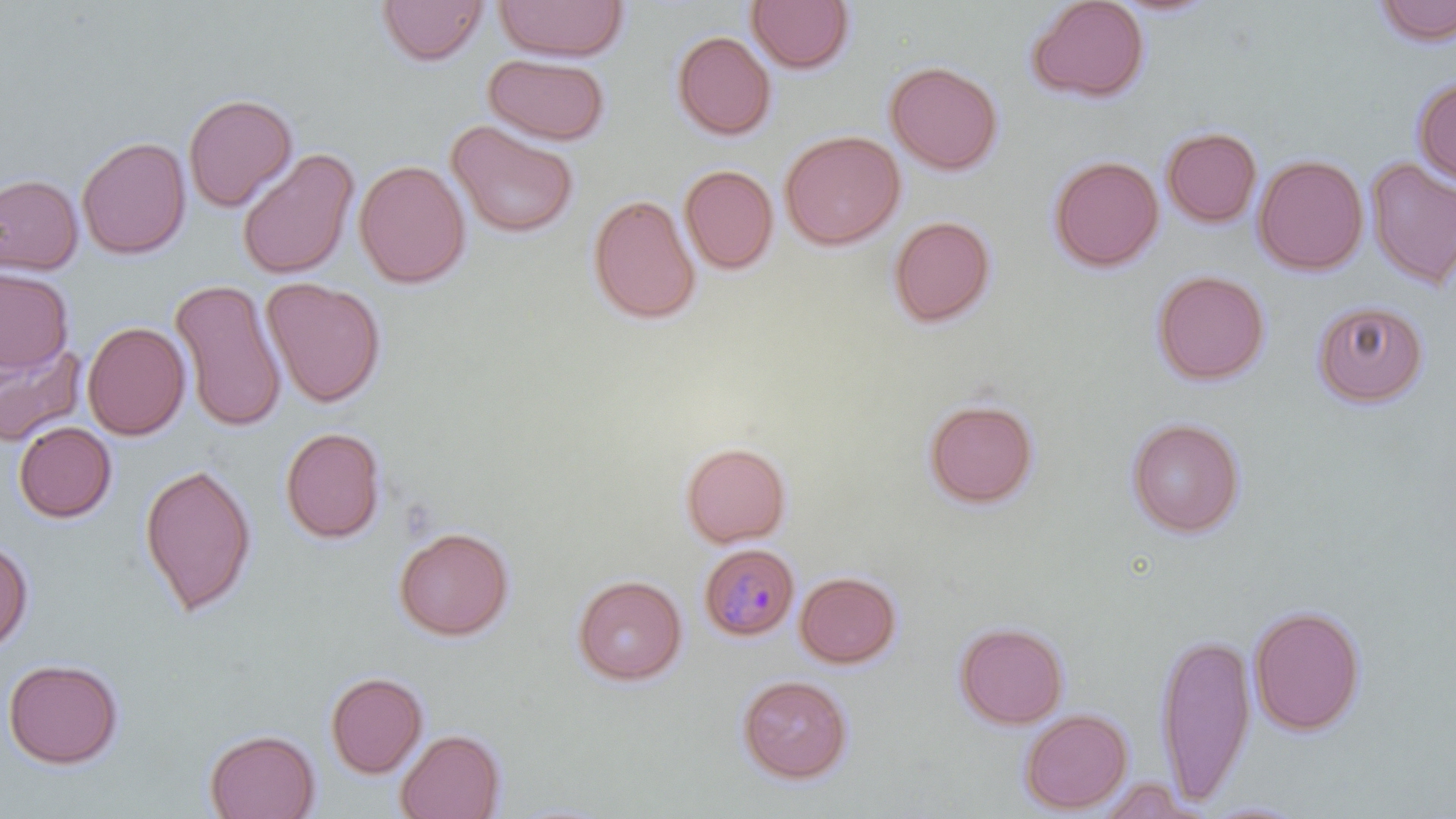
slide-level diagnosis = Plasmodium malariae
field of view = single
magnification = 1000x
uninfected red blood cell locations = approximate bounding boxes as named x1/y1/x2/y2 corners in pixels: (x1=376, y1=0, x2=489, y2=66), (x1=492, y1=0, x2=629, y2=62), (x1=1025, y1=0, x2=1150, y2=104), (x1=745, y1=1, x2=855, y2=74), (x1=1104, y1=1, x2=1224, y2=20), (x1=1371, y1=1, x2=1456, y2=47), (x1=671, y1=30, x2=777, y2=141), (x1=483, y1=54, x2=611, y2=145), (x1=885, y1=60, x2=1003, y2=176), (x1=1412, y1=75, x2=1456, y2=186), (x1=183, y1=92, x2=298, y2=212), (x1=445, y1=120, x2=580, y2=239), (x1=1161, y1=126, x2=1262, y2=228), (x1=779, y1=129, x2=906, y2=250), (x1=77, y1=135, x2=191, y2=259), (x1=236, y1=148, x2=360, y2=280), (x1=1252, y1=154, x2=1369, y2=276), (x1=1048, y1=155, x2=1164, y2=273), (x1=1365, y1=157, x2=1456, y2=290), (x1=354, y1=159, x2=471, y2=289), (x1=679, y1=164, x2=778, y2=274), (x1=0, y1=173, x2=83, y2=276), (x1=587, y1=193, x2=702, y2=325), (x1=888, y1=215, x2=997, y2=328), (x1=0, y1=268, x2=74, y2=373), (x1=1151, y1=269, x2=1270, y2=386), (x1=261, y1=277, x2=386, y2=407), (x1=170, y1=278, x2=287, y2=433), (x1=1311, y1=299, x2=1428, y2=407), (x1=82, y1=320, x2=191, y2=440), (x1=0, y1=338, x2=86, y2=447), (x1=923, y1=398, x2=1039, y2=509), (x1=1125, y1=417, x2=1246, y2=538), (x1=13, y1=421, x2=117, y2=523), (x1=279, y1=426, x2=387, y2=544), (x1=680, y1=441, x2=792, y2=548), (x1=138, y1=462, x2=258, y2=618), (x1=393, y1=526, x2=515, y2=642), (x1=0, y1=537, x2=35, y2=654), (x1=794, y1=570, x2=902, y2=669), (x1=572, y1=573, x2=687, y2=686), (x1=1248, y1=604, x2=1366, y2=736), (x1=954, y1=621, x2=1068, y2=729), (x1=1155, y1=629, x2=1256, y2=806), (x1=2, y1=657, x2=124, y2=769), (x1=324, y1=670, x2=429, y2=778), (x1=736, y1=674, x2=854, y2=784), (x1=1019, y1=707, x2=1133, y2=813), (x1=204, y1=728, x2=321, y2=819), (x1=394, y1=728, x2=506, y2=819)
stain = May-Grünwald-Giemsa
Plasmodium malariae-infected red blood cell locations = approximate bounding boxes as named x1/y1/x2/y2 corners in pixels: (x1=698, y1=543, x2=800, y2=641)
preparation = thin blood smear
image size = 1456×819 pixels
modality = light microscopy